Report the malaria status of this cell.
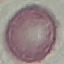

It is uninfected.

Photographed with a smartphone camera at the microscope eyepiece. Giemsa stain. Automatically extracted cell patch, resized to 64 × 64 pixels. Thin blood film.